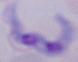

{
  "magnification": "1000x",
  "modality": "photomicrograph",
  "identification": "trypanosome"
}